Give the position of every Plasmodium parasite.
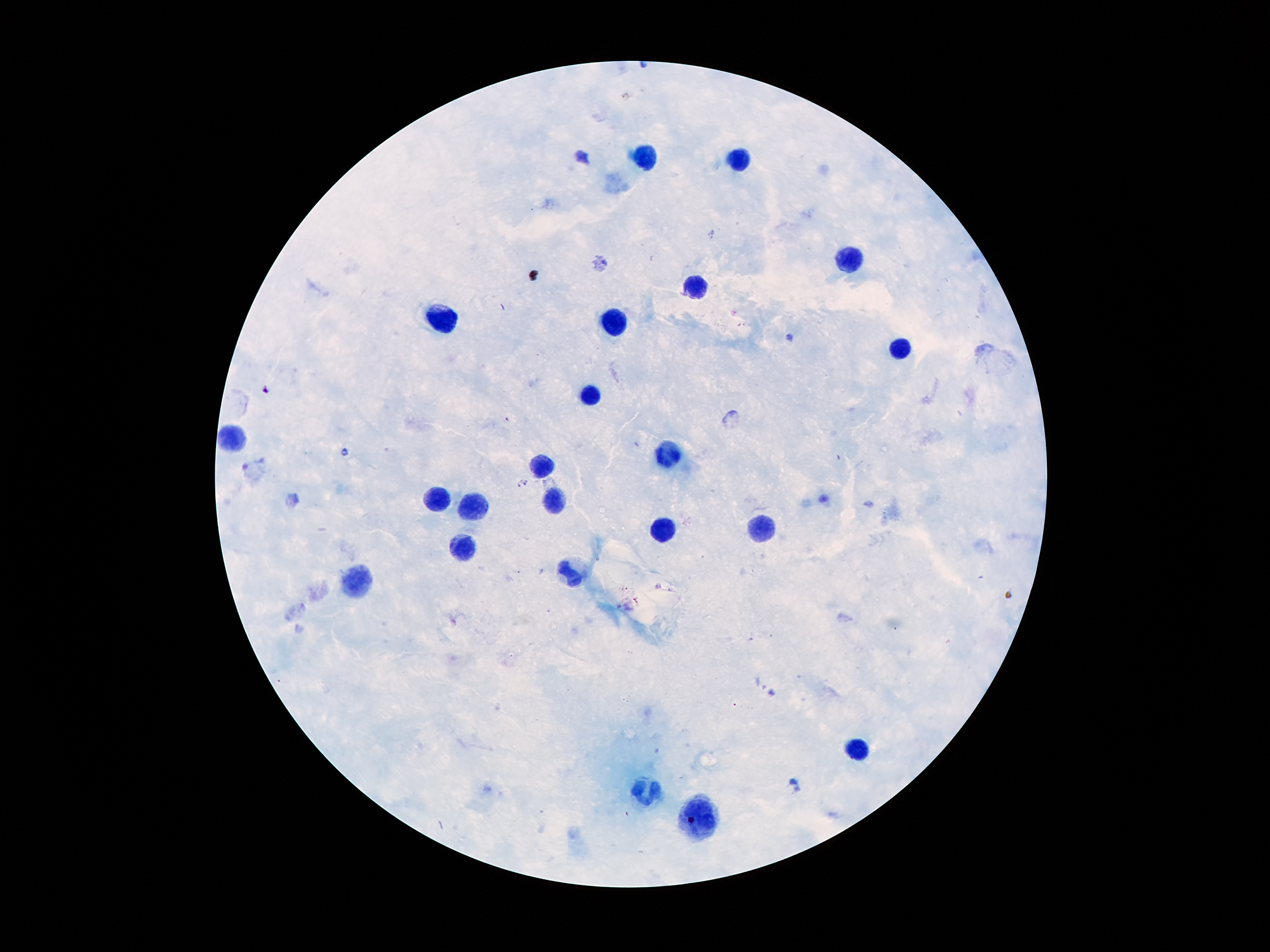
Approximate centers as [x, y] in pixels.
Plasmodium parasites: [788, 337], [266, 389], [345, 452], [521, 482].

Leukocyte locations: [643, 157], [739, 158], [849, 263], [693, 284], [441, 321], [618, 328], [901, 349], [590, 389], [232, 438], [672, 459], [538, 468], [439, 500], [549, 501], [479, 508], [658, 531], [765, 531], [460, 548], [572, 569], [358, 584], [857, 750], [643, 793], [702, 820]. Thick blood smear. 100x magnification. Patient malaria status: infected with Plasmodium falciparum. Giemsa-stained preparation. Image is 1270×952 pixels. One field from this slide. Smartphone photograph taken through the microscope eyepiece.